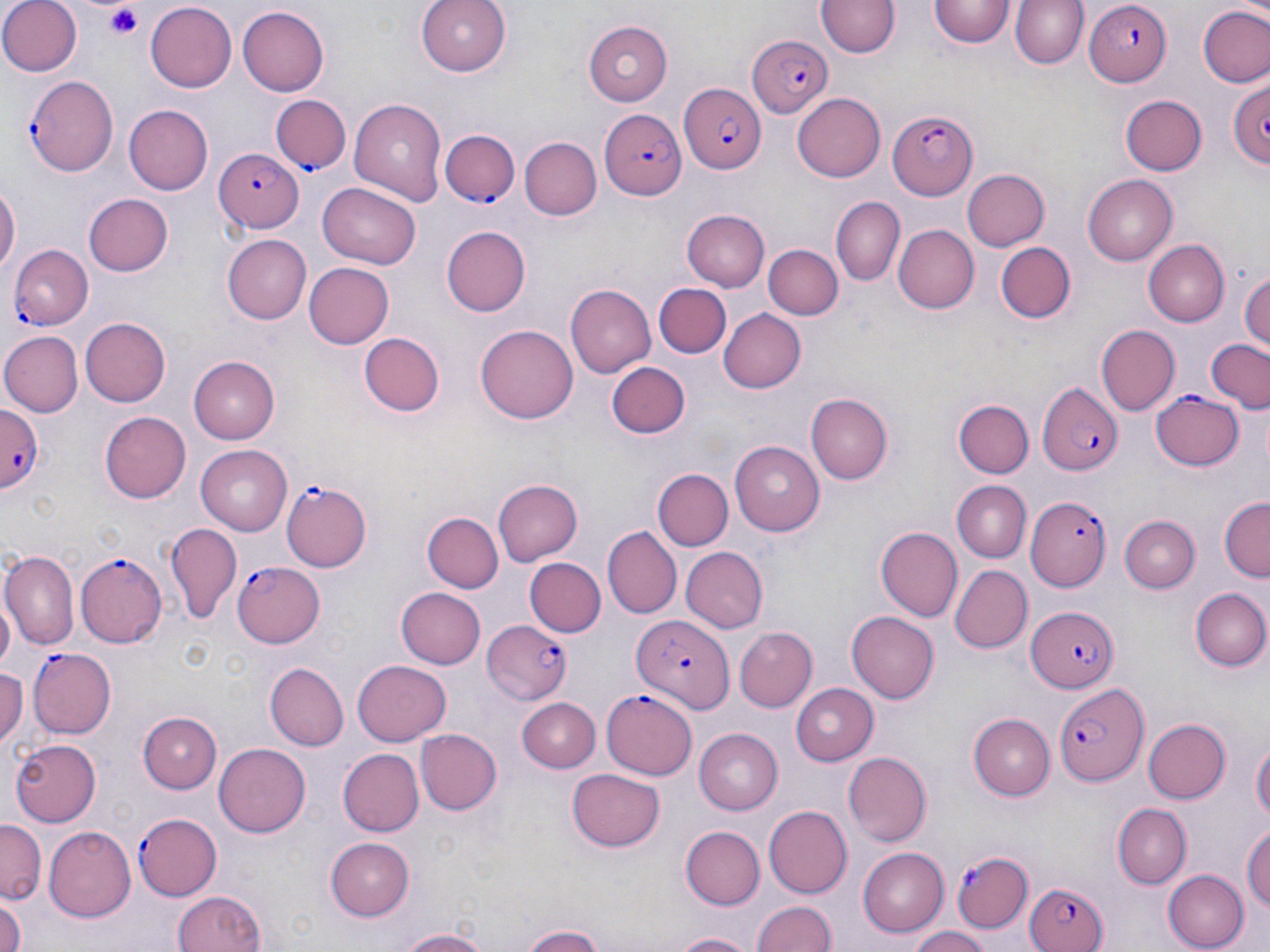
Approximate bounding boxes as (x1, y1, x2, y2) in pixels. Platelet locations: (106, 6, 145, 39). Uninfected red blood cell locations: (0, 0, 80, 75), (418, 0, 514, 73), (817, 1, 898, 57), (930, 1, 1014, 50), (1010, 1, 1088, 71), (144, 3, 237, 93), (1200, 5, 1270, 89), (236, 6, 330, 97), (583, 20, 671, 104), (1227, 76, 1270, 168), (792, 92, 885, 182), (1120, 95, 1208, 176), (350, 99, 450, 202), (123, 104, 212, 195), (520, 138, 602, 221), (963, 167, 1051, 250), (1083, 175, 1179, 265), (318, 184, 422, 269), (0, 186, 18, 278), (83, 193, 173, 276), (831, 198, 903, 285), (680, 209, 770, 290), (440, 225, 529, 316), (893, 226, 978, 311), (222, 235, 310, 324), (994, 240, 1078, 325), (1141, 240, 1227, 326), (762, 243, 842, 321), (304, 264, 394, 348), (1243, 268, 1270, 352), (565, 282, 656, 376), (654, 283, 730, 359), (719, 310, 809, 393), (80, 317, 171, 406), (475, 324, 579, 423), (1095, 325, 1179, 417), (0, 331, 81, 417), (360, 331, 445, 416), (1207, 339, 1269, 412), (189, 356, 280, 444), (608, 363, 691, 439), (805, 393, 893, 485), (954, 398, 1033, 478), (100, 412, 191, 502), (732, 440, 824, 535), (196, 443, 292, 533), (653, 469, 732, 552), (493, 478, 583, 564), (951, 480, 1030, 560), (1219, 496, 1270, 581), (424, 513, 503, 594), (1121, 514, 1199, 593), (162, 525, 241, 621), (875, 527, 963, 621), (601, 528, 681, 616), (680, 547, 767, 631), (1, 550, 79, 651), (525, 557, 605, 638), (948, 564, 1032, 654), (381, 584, 474, 740), (395, 588, 486, 669), (1189, 588, 1270, 671), (0, 590, 16, 676), (848, 612, 938, 704), (735, 628, 815, 710), (354, 659, 451, 744), (265, 663, 349, 751), (0, 666, 25, 748), (788, 683, 880, 762), (520, 699, 601, 771), (140, 711, 222, 794), (968, 713, 1055, 800), (1142, 719, 1228, 804), (415, 728, 501, 815), (692, 728, 783, 815), (1251, 737, 1269, 828), (9, 739, 102, 827), (214, 743, 309, 838), (337, 747, 426, 838), (842, 750, 931, 847), (567, 769, 665, 852), (1112, 804, 1190, 888), (763, 805, 852, 898), (0, 822, 44, 903), (43, 826, 135, 921), (678, 826, 765, 911), (1242, 826, 1270, 912), (327, 835, 415, 920), (857, 847, 949, 936), (1163, 867, 1246, 950), (169, 891, 266, 952), (0, 892, 26, 952), (752, 898, 838, 952), (523, 924, 610, 952), (906, 925, 991, 952), (392, 927, 494, 952), (668, 931, 756, 952). Plasmodium falciparum-infected red blood cell locations: (1084, 3, 1170, 85), (746, 36, 831, 118), (25, 75, 118, 177), (677, 84, 766, 174), (271, 95, 350, 174), (886, 109, 977, 201), (598, 110, 686, 199), (441, 128, 519, 205), (214, 148, 304, 232), (10, 245, 94, 328), (1038, 383, 1122, 477), (1152, 388, 1245, 470), (0, 403, 44, 491), (281, 480, 371, 573), (1028, 494, 1114, 588), (74, 550, 166, 645), (233, 560, 325, 646), (1026, 603, 1118, 691), (631, 614, 733, 713), (481, 618, 571, 705), (27, 647, 117, 737), (1058, 682, 1152, 787), (602, 687, 699, 780), (131, 813, 224, 897), (949, 850, 1035, 935), (1027, 883, 1110, 952). Slide-level diagnosis: Plasmodium falciparum. Image is 1270×952 pixels. May-Grünwald-Giemsa stain. Single field of view. Optical microscopy. Captured at 1000x magnification. Thin blood film.